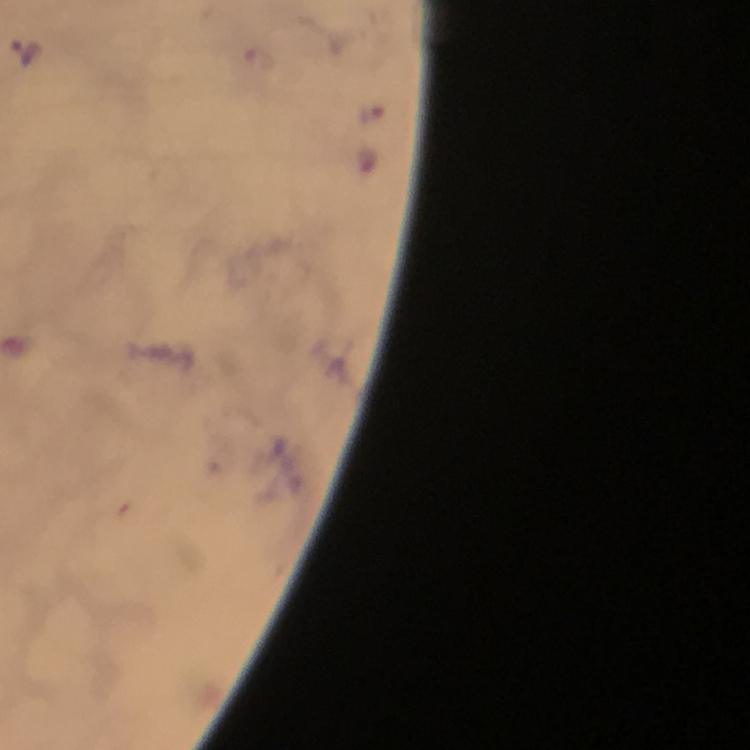

capture = smartphone camera through the microscope
immersion oil = used
preparation = thick smear
stain = Giemsa
magnification = 100x
context = from a malaria diagnostic workup
Plasmodium parasite locations = approximate centers as [x, y] in pixels: [27, 51], [258, 62], [370, 113]
cropped from = one field of view
image size = 750×750 pixels